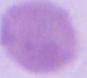

Summary:
  - Modality: photomicrograph
  - Identification: erythrocyte
  - Magnification: 1000x